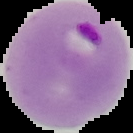
Summary:
  - Preparation: thin blood film
  - Image type: cell region segmented out of the field of view; surrounding area masked to black
  - Image size: 133×133 pixels
  - Malaria status: parasitized